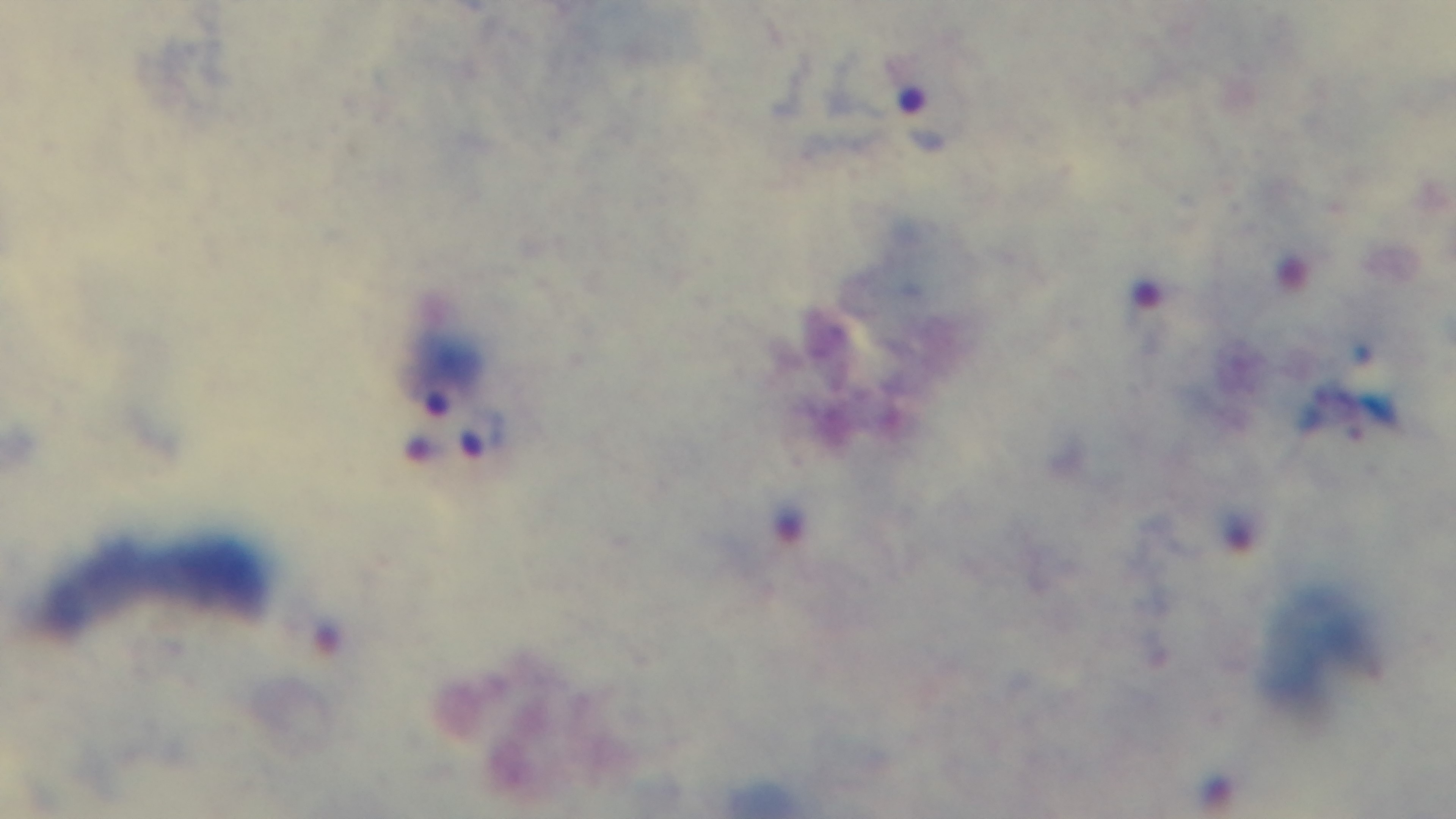
Preparation: thick. Malaria status: positive. Light microscopy. Mounted 4K digital camera. Giemsa-stained. Oil-immersion objective, 100x. Single field of view.